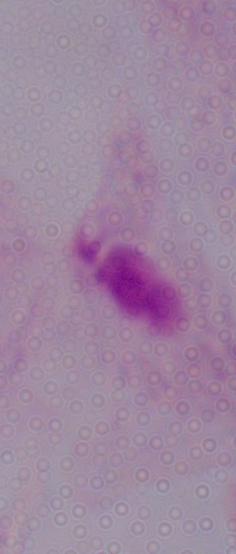
modality = photomicrograph
identification = trichomonad
magnification = 1000x